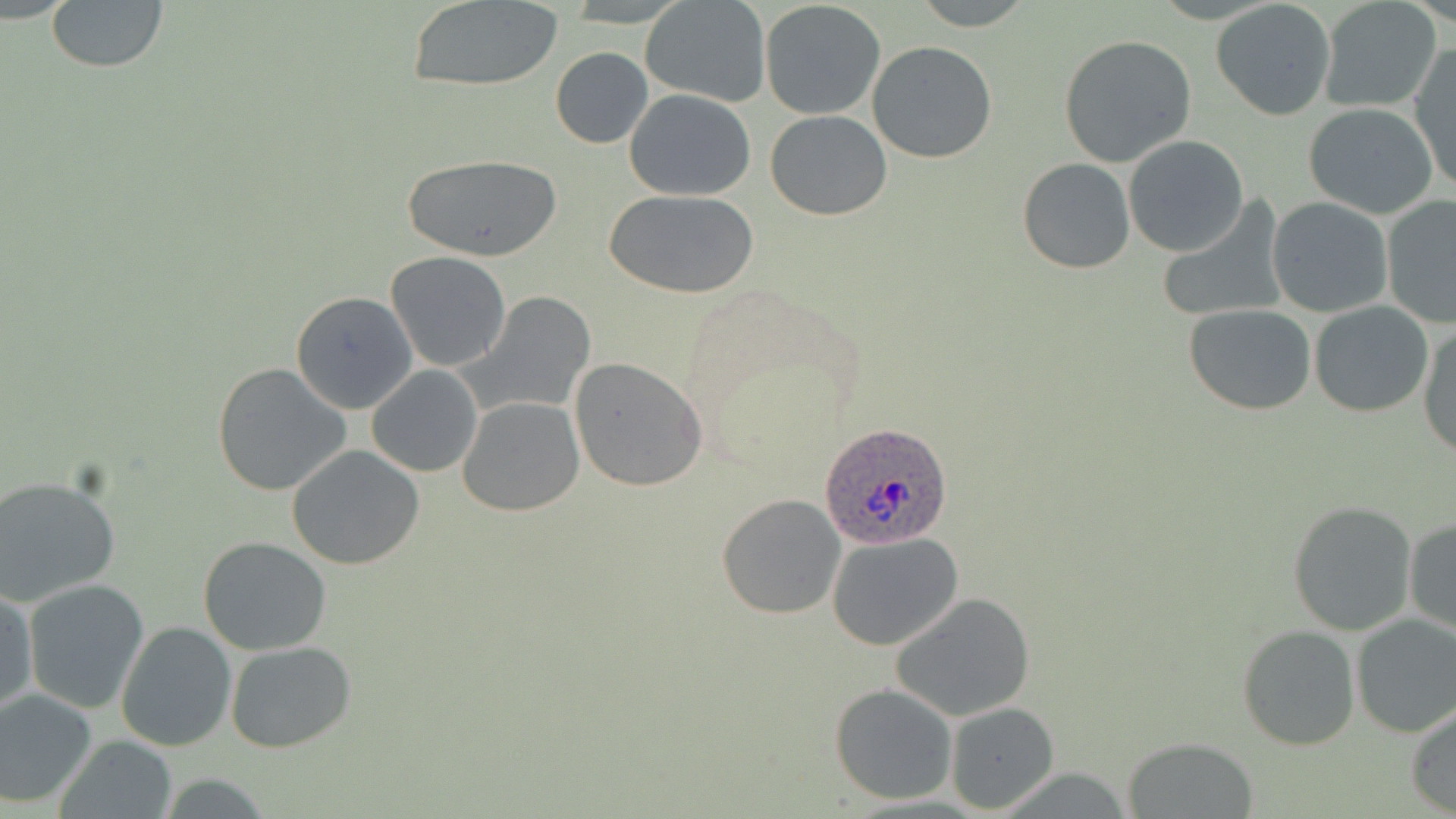

{
  "slide_level_diagnosis": "Plasmodium ovale",
  "field_of_view": "single",
  "image_size": "1456×819 pixels",
  "preparation": "thin blood film",
  "magnification": "1000x",
  "modality": "light microscopy",
  "stain": "May-Grünwald-Giemsa",
  "uninfected_red_blood_cell_locations": "approximate bounding boxes as named x1/y1/x2/y2 corners in pixels: (x1=45, y1=0, x2=168, y2=72), (x1=1318, y1=0, x2=1442, y2=113), (x1=408, y1=1, x2=563, y2=90), (x1=641, y1=1, x2=770, y2=106), (x1=905, y1=2, x2=1043, y2=30), (x1=1210, y1=2, x2=1337, y2=121), (x1=759, y1=3, x2=882, y2=120), (x1=1058, y1=34, x2=1198, y2=168), (x1=867, y1=40, x2=997, y2=164), (x1=1408, y1=45, x2=1456, y2=192), (x1=550, y1=47, x2=653, y2=149), (x1=624, y1=88, x2=757, y2=200), (x1=1303, y1=103, x2=1440, y2=219), (x1=766, y1=109, x2=892, y2=221), (x1=1123, y1=135, x2=1249, y2=257), (x1=401, y1=152, x2=561, y2=261), (x1=1017, y1=157, x2=1137, y2=274), (x1=605, y1=188, x2=760, y2=299), (x1=1267, y1=197, x2=1394, y2=319), (x1=1381, y1=197, x2=1455, y2=327), (x1=1158, y1=199, x2=1290, y2=325), (x1=385, y1=252, x2=511, y2=372), (x1=290, y1=291, x2=417, y2=413), (x1=463, y1=291, x2=595, y2=414), (x1=1309, y1=301, x2=1435, y2=418), (x1=1185, y1=305, x2=1317, y2=415), (x1=1419, y1=324, x2=1456, y2=458), (x1=570, y1=358, x2=707, y2=491), (x1=211, y1=364, x2=352, y2=499), (x1=367, y1=365, x2=482, y2=476), (x1=457, y1=396, x2=584, y2=517), (x1=287, y1=444, x2=425, y2=570), (x1=0, y1=475, x2=121, y2=607), (x1=717, y1=493, x2=845, y2=618), (x1=1286, y1=500, x2=1418, y2=635), (x1=1404, y1=515, x2=1455, y2=639), (x1=827, y1=531, x2=963, y2=651), (x1=196, y1=536, x2=334, y2=656), (x1=22, y1=578, x2=149, y2=713), (x1=1, y1=587, x2=36, y2=719), (x1=891, y1=593, x2=1036, y2=721), (x1=1350, y1=615, x2=1456, y2=738), (x1=115, y1=621, x2=236, y2=752), (x1=1237, y1=626, x2=1360, y2=749), (x1=224, y1=640, x2=354, y2=753), (x1=830, y1=682, x2=958, y2=804), (x1=0, y1=691, x2=97, y2=808), (x1=946, y1=703, x2=1057, y2=812), (x1=1406, y1=703, x2=1456, y2=816), (x1=56, y1=735, x2=177, y2=819), (x1=1123, y1=736, x2=1260, y2=818)",
  "plasmodium_ovale_infected_red_blood_cell_locations": "approximate bounding boxes as named x1/y1/x2/y2 corners in pixels: (x1=822, y1=424, x2=951, y2=546)"
}